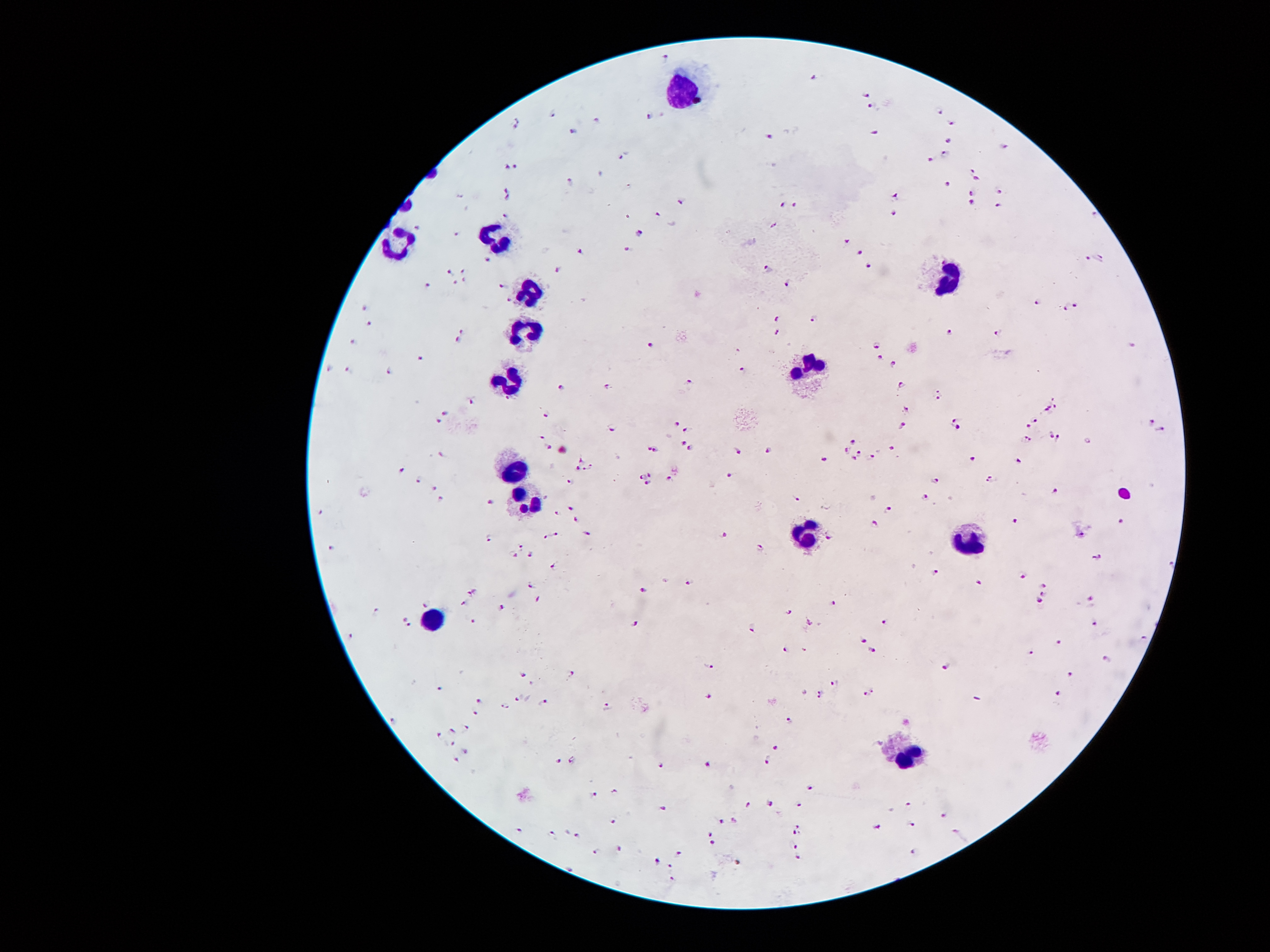
coordinate format = approximate centers as [x, y] in pixels
malaria parasite locations = [664, 58], [815, 78], [865, 94], [871, 107], [940, 112], [552, 113], [649, 116], [516, 120], [593, 120], [951, 124], [574, 131], [875, 131], [767, 136], [948, 142], [1004, 145], [946, 154], [621, 157], [930, 158], [517, 164], [507, 167], [972, 171], [571, 179], [977, 181], [947, 186], [509, 191], [1000, 192], [971, 193], [895, 196], [506, 198], [682, 201], [970, 204], [782, 205], [794, 206], [997, 207], [659, 214], [890, 214], [504, 215], [1092, 215], [415, 227], [457, 233], [636, 234], [844, 242], [629, 250], [582, 251], [860, 252], [1098, 256], [1087, 259], [488, 260], [768, 267], [869, 267], [558, 269], [464, 270], [449, 272], [464, 280], [425, 282], [455, 282], [788, 283], [501, 286], [508, 301], [1039, 302], [1077, 306], [1067, 307], [364, 308], [777, 319], [814, 320], [371, 324], [460, 326], [948, 331], [778, 332], [998, 334], [458, 340], [356, 342], [651, 343], [878, 344], [1131, 345], [419, 358], [880, 358], [894, 364], [328, 368], [350, 370], [390, 371], [742, 371], [691, 383], [902, 386], [564, 388], [609, 388], [936, 398], [1053, 398], [472, 403], [1055, 407], [907, 408], [1048, 408], [446, 411], [544, 415], [956, 418], [438, 421], [1036, 421], [676, 423], [1152, 423], [1028, 424], [902, 426], [613, 427], [955, 428], [686, 429], [1162, 430], [541, 435], [1049, 436], [1059, 437], [1029, 440], [683, 442], [854, 442], [546, 445], [649, 449], [690, 449], [656, 450], [846, 450], [738, 451], [768, 451], [891, 451], [860, 453], [442, 455], [855, 458], [871, 458], [581, 459], [825, 459], [973, 459], [1019, 461], [589, 468], [576, 469], [403, 470], [650, 474], [729, 475], [640, 476], [670, 477], [990, 479], [419, 480], [570, 481], [935, 481], [648, 484], [433, 487], [1054, 490], [925, 496], [796, 498], [441, 500], [492, 503], [572, 508], [889, 508], [558, 512], [1015, 519], [575, 520], [1123, 521], [873, 526], [558, 533], [588, 534], [726, 534], [544, 535], [490, 538], [1083, 538], [831, 539], [523, 546], [332, 549], [761, 549], [512, 553], [530, 555], [1104, 557], [1169, 563], [556, 566], [935, 573], [1024, 575], [688, 582], [979, 582], [530, 585], [1044, 585], [644, 589], [472, 593], [1043, 595], [538, 600], [1093, 600], [1038, 601], [462, 603], [835, 603], [423, 606], [502, 608], [377, 610], [789, 612], [402, 616], [474, 621], [809, 622], [884, 622], [1092, 622], [634, 625], [410, 626], [753, 627], [350, 637], [863, 641], [1061, 642], [872, 648], [784, 649], [1033, 651], [1107, 657], [708, 665], [948, 666], [571, 673], [525, 674], [1070, 676], [834, 682], [440, 688], [821, 692], [870, 692], [1058, 693], [706, 694], [519, 698], [480, 700], [543, 702], [506, 706], [607, 707], [478, 715], [396, 720], [791, 721], [466, 728], [451, 730], [438, 735], [451, 743], [777, 748], [465, 752], [455, 759], [574, 759], [767, 760], [559, 761], [707, 764], [660, 766], [812, 789], [615, 791], [594, 792], [798, 804], [908, 804], [771, 805], [750, 806], [661, 808], [943, 816], [735, 820], [614, 822], [723, 822], [910, 824], [798, 825], [876, 828], [518, 829], [551, 832], [794, 832], [957, 832], [711, 833], [578, 835], [714, 842], [796, 845], [619, 849], [596, 852], [912, 853], [679, 855], [796, 858], [657, 860], [671, 867], [570, 868], [671, 879]
leukocyte locations = [685, 89], [496, 235], [395, 245], [948, 283], [533, 290], [526, 333], [810, 366], [509, 384], [511, 470], [524, 499], [806, 534], [965, 536], [432, 620], [909, 756]
image size = 1270×952 pixels
magnification = 100x
capture = smartphone camera through the microscope eyepiece
preparation = thick blood film
patient malaria status = positive for Plasmodium falciparum
field of view = single
stain = Giemsa